Identify the parasite.
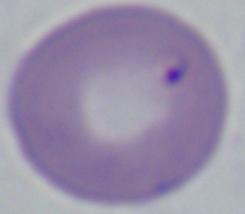
This is Babesia.

magnification = 1000x
modality = micrograph